Report the malaria status of this cell.
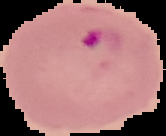
It is parasitized.

From a thin blood film. Image is 166×136 pixels. Cell region segmented out of the field of view; the surrounding area is masked to black.